Give the preparation type.
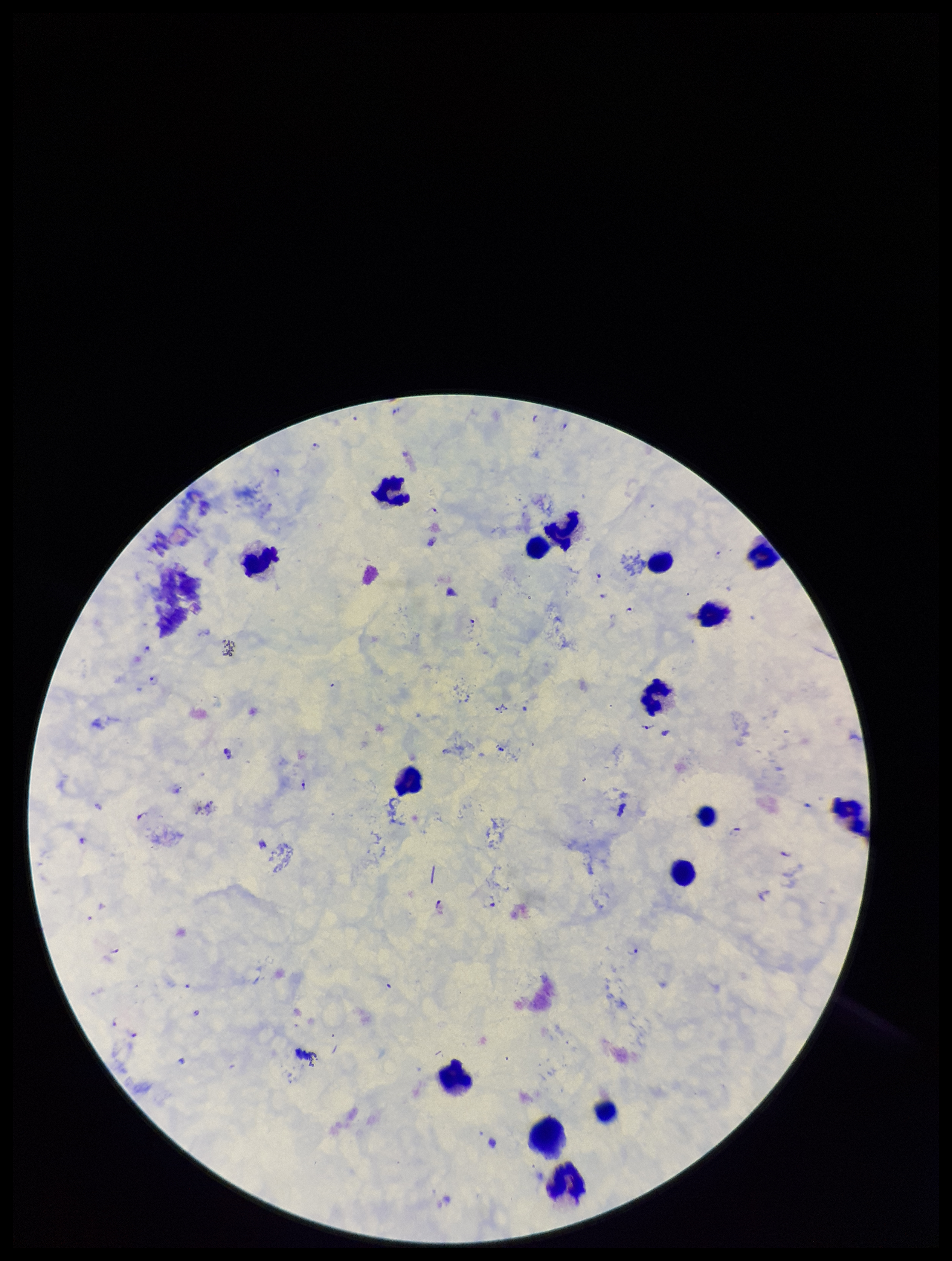

A thick smear.

Parasite count: 26. Image is 952×1261 pixels. Smartphone photograph taken through the eyepiece of a microscope. Leukocyte count: 16. Stained with Giemsa. One field from this slide. Patient malaria status: infected. Plasmodium parasites: seen. Species reported for this patient: Plasmodium falciparum.